Report the malaria status of this cell.
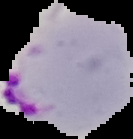
Parasitized.

preparation = thin blood smear
image size = 133×139 pixels
image type = segmented cell region with the area outside set to black